Name the parasite shown.
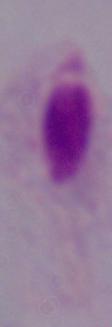

This is a trichomonad.

1000x magnification. Micrograph.